State which parasite is depicted.
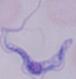

A trypanosome.

{
  "magnification": "1000x",
  "modality": "photomicrograph"
}